Identify the blood parasite species.
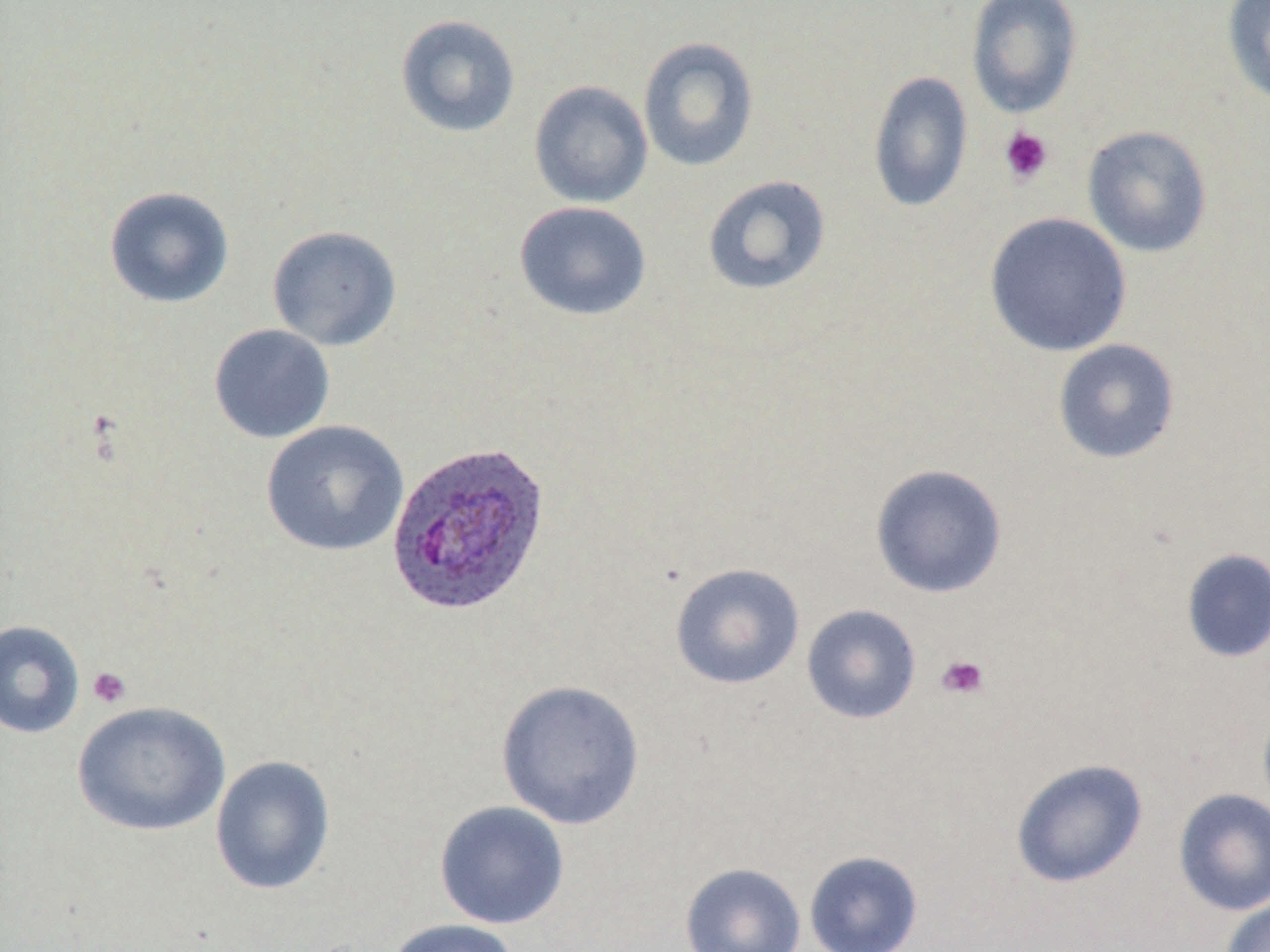

Plasmodium ovale.

Approximate bounding boxes as (x1, y1, x2, y2) in pixels. Platelet locations: (999, 127, 1054, 185), (935, 654, 990, 700), (87, 666, 131, 708). Uninfected red blood cell locations: (966, 1, 1083, 119), (1222, 1, 1270, 106), (395, 13, 521, 138), (637, 36, 760, 172), (867, 70, 974, 213), (528, 80, 653, 208), (1082, 125, 1213, 258), (702, 175, 831, 296), (103, 185, 235, 309), (514, 200, 651, 321), (984, 212, 1132, 358), (266, 225, 403, 351), (208, 324, 335, 443), (1052, 338, 1180, 464), (260, 420, 409, 557), (869, 463, 1008, 599), (1180, 548, 1270, 665), (669, 562, 805, 690), (801, 604, 922, 724), (0, 620, 85, 739), (495, 679, 645, 830), (1257, 699, 1270, 821), (71, 701, 231, 837), (211, 755, 335, 896), (1010, 758, 1148, 888), (1172, 788, 1270, 916), (434, 800, 570, 929), (804, 850, 923, 952), (680, 862, 806, 952), (1219, 895, 1270, 952), (381, 918, 523, 952). Plasmodium ovale-infected red blood cell locations: (385, 440, 551, 617). Light microscopy. Thin blood smear. May-Grünwald-Giemsa stain. 1000x magnification. Image is 1270×952 pixels. Single field of view.